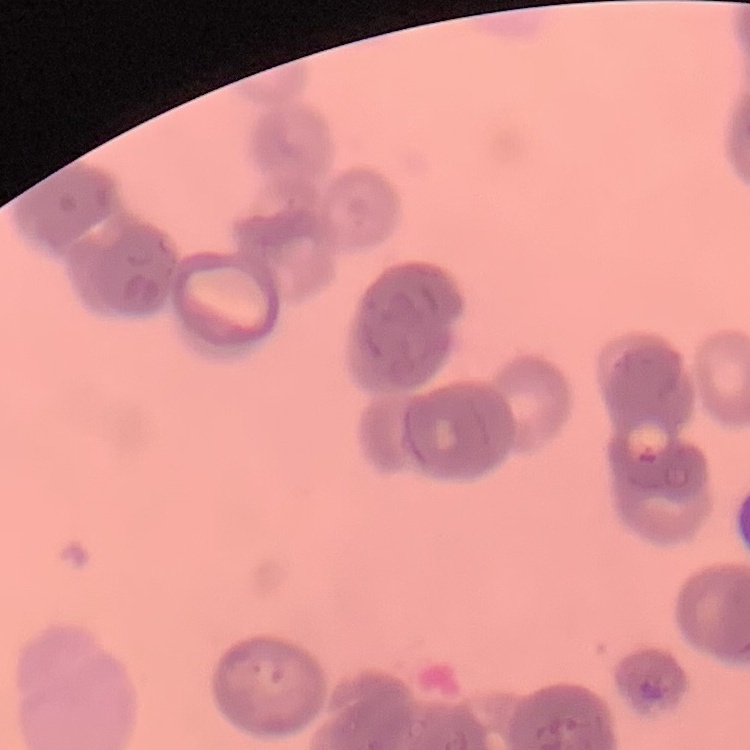
The red blood cells show rouleaux formation. Thin peripheral smear. Stained with either Field's or Giemsa. One tile cut from a larger photomicrograph.